Outline each Plasmodium vivax-infected red blood cell.
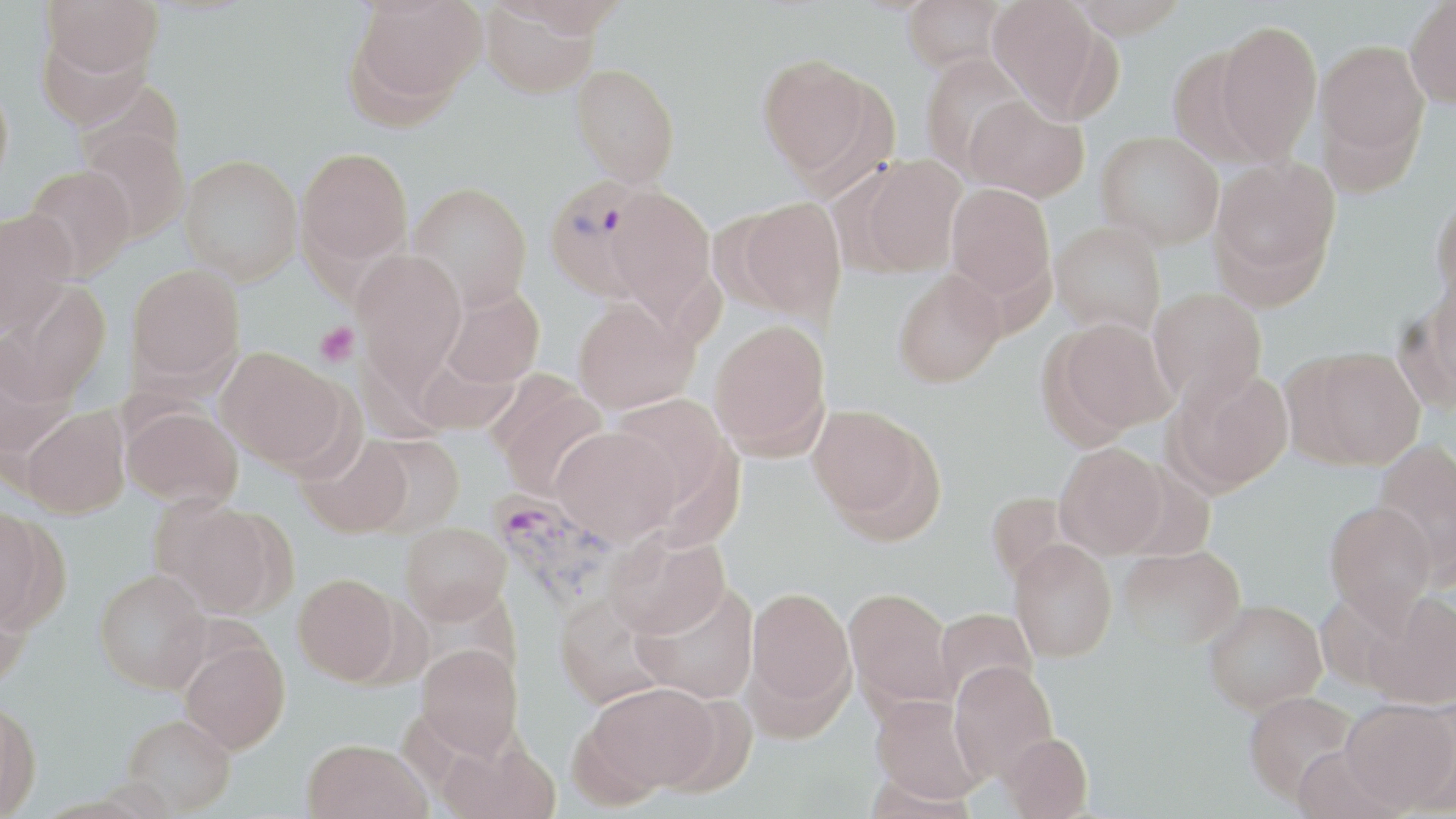
Approximate bounding boxes as named x1/y1/x2/y2 corners in pixels.
Plasmodium vivax-infected red blood cells: (x1=544, y1=176, x2=661, y2=301), (x1=490, y1=489, x2=622, y2=614).

Summary:
  - Platelet locations: (x1=314, y1=321, x2=360, y2=367)
  - Uninfected red blood cell locations: (x1=347, y1=0, x2=485, y2=117), (x1=901, y1=0, x2=1008, y2=73), (x1=988, y1=0, x2=1108, y2=119), (x1=1066, y1=0, x2=1191, y2=38), (x1=1405, y1=0, x2=1456, y2=108), (x1=42, y1=1, x2=163, y2=79), (x1=481, y1=2, x2=600, y2=98), (x1=1214, y1=20, x2=1323, y2=162), (x1=35, y1=28, x2=154, y2=127), (x1=1314, y1=39, x2=1430, y2=175), (x1=1167, y1=46, x2=1273, y2=167), (x1=919, y1=53, x2=1032, y2=178), (x1=756, y1=54, x2=880, y2=180), (x1=571, y1=63, x2=680, y2=186), (x1=0, y1=78, x2=13, y2=198), (x1=964, y1=95, x2=1089, y2=202), (x1=77, y1=122, x2=190, y2=243), (x1=1096, y1=132, x2=1223, y2=250), (x1=297, y1=147, x2=413, y2=270), (x1=179, y1=154, x2=303, y2=284), (x1=853, y1=155, x2=967, y2=276), (x1=1211, y1=157, x2=1339, y2=288), (x1=21, y1=164, x2=137, y2=281), (x1=408, y1=181, x2=532, y2=312), (x1=607, y1=183, x2=715, y2=320), (x1=946, y1=183, x2=1056, y2=302), (x1=1431, y1=193, x2=1456, y2=303), (x1=730, y1=197, x2=846, y2=320), (x1=0, y1=210, x2=75, y2=336), (x1=1050, y1=221, x2=1165, y2=337), (x1=351, y1=250, x2=467, y2=382), (x1=125, y1=263, x2=245, y2=386), (x1=893, y1=269, x2=1006, y2=388), (x1=1422, y1=270, x2=1456, y2=404), (x1=3, y1=281, x2=111, y2=406), (x1=441, y1=287, x2=544, y2=389), (x1=1148, y1=288, x2=1268, y2=407), (x1=572, y1=296, x2=698, y2=413), (x1=1047, y1=317, x2=1175, y2=436), (x1=709, y1=318, x2=831, y2=458), (x1=217, y1=347, x2=351, y2=469), (x1=1291, y1=347, x2=1426, y2=469), (x1=1168, y1=368, x2=1294, y2=494), (x1=489, y1=378, x2=609, y2=497), (x1=609, y1=394, x2=731, y2=507), (x1=808, y1=404, x2=941, y2=536), (x1=122, y1=405, x2=243, y2=508), (x1=19, y1=406, x2=130, y2=518), (x1=551, y1=426, x2=683, y2=543), (x1=362, y1=433, x2=465, y2=536), (x1=298, y1=434, x2=412, y2=539), (x1=1372, y1=438, x2=1456, y2=574), (x1=1055, y1=443, x2=1169, y2=559), (x1=985, y1=490, x2=1071, y2=587), (x1=159, y1=500, x2=290, y2=618), (x1=1324, y1=501, x2=1438, y2=622), (x1=0, y1=505, x2=52, y2=632), (x1=400, y1=522, x2=511, y2=623), (x1=605, y1=529, x2=729, y2=638), (x1=1010, y1=540, x2=1117, y2=662), (x1=1119, y1=545, x2=1245, y2=651), (x1=94, y1=569, x2=211, y2=693), (x1=293, y1=573, x2=400, y2=684), (x1=632, y1=581, x2=759, y2=704), (x1=0, y1=585, x2=30, y2=690), (x1=746, y1=586, x2=855, y2=720), (x1=844, y1=586, x2=958, y2=710), (x1=1365, y1=591, x2=1456, y2=709), (x1=553, y1=593, x2=670, y2=709), (x1=1204, y1=599, x2=1326, y2=713), (x1=934, y1=606, x2=1037, y2=702), (x1=180, y1=638, x2=290, y2=754), (x1=416, y1=643, x2=523, y2=758), (x1=949, y1=661, x2=1058, y2=783), (x1=588, y1=681, x2=721, y2=794), (x1=1244, y1=690, x2=1359, y2=803), (x1=870, y1=695, x2=986, y2=803), (x1=0, y1=698, x2=42, y2=817), (x1=1341, y1=698, x2=1456, y2=812), (x1=121, y1=714, x2=236, y2=814), (x1=1000, y1=732, x2=1093, y2=819), (x1=301, y1=738, x2=429, y2=819), (x1=1291, y1=745, x2=1406, y2=818)
  - Slide-level diagnosis: Plasmodium vivax
  - Field of view: one of a larger specimen
  - Image size: 1456×819 pixels
  - Preparation: thin blood smear
  - Modality: optical microscopy
  - Stain: May-Grünwald-Giemsa
  - Magnification: 1000x